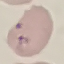

{
  "malaria_status": "parasitized",
  "image_type": "cell patch, automatically extracted from a larger field of view and resized to 64 × 64 pixels",
  "stain": "Giemsa",
  "capture": "smartphone through the microscope eyepiece",
  "preparation": "thin smear"
}